Evaluate for malaria.
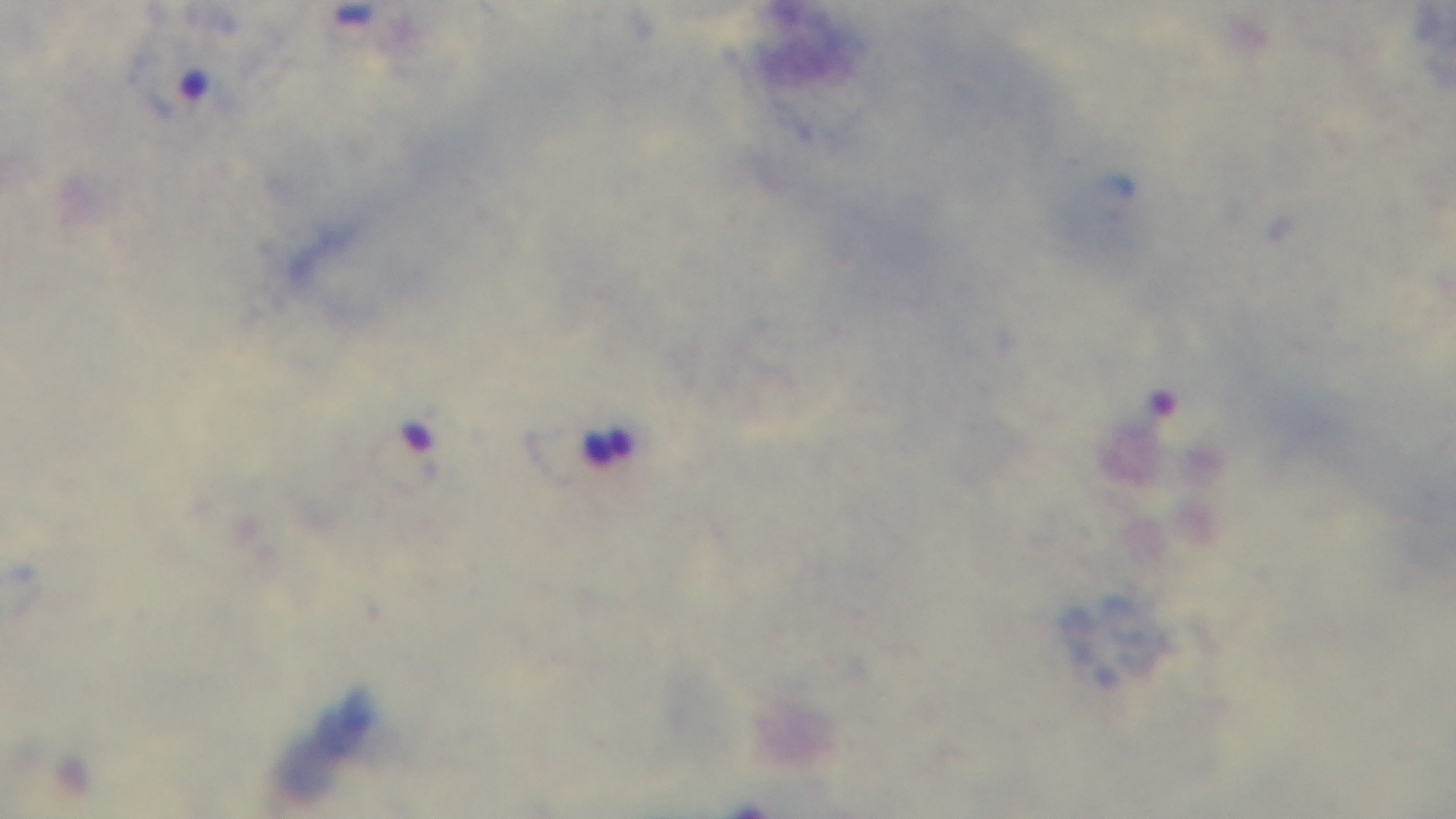
It is infected.

Photomicrograph. Preparation: thick blood film. Giemsa stain. Oil-immersion objective, 100x. One field from the slide. Mounted 4K digital camera.